Classify this cell by malaria status.
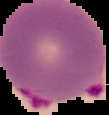

Parasitized.

preparation = thin blood film
image type = cell region segmented out of the field of view; surrounding area masked to black
image size = 109×115 pixels